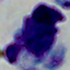 Micrograph. A leukocyte is shown. Captured at 1000x magnification.